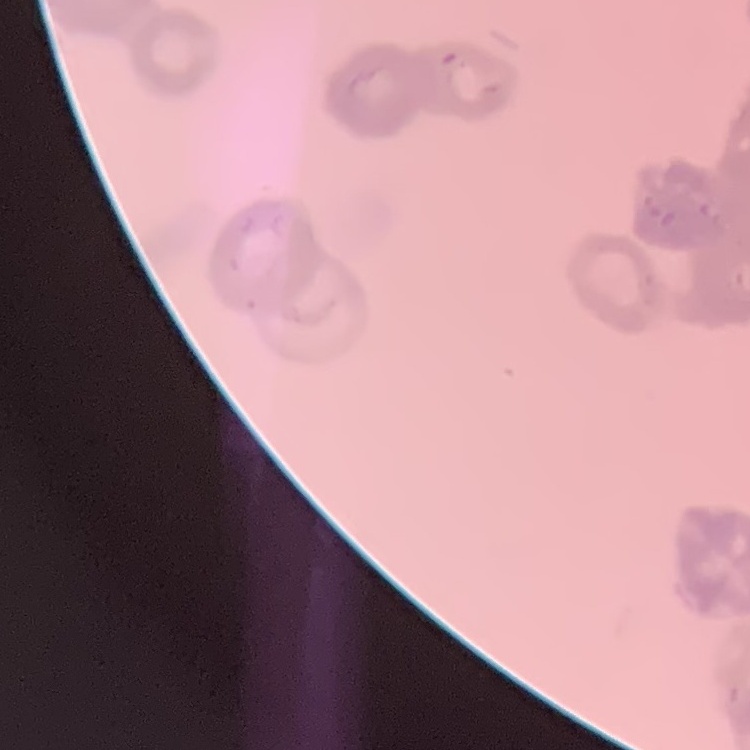
Summary:
  - Red blood cell morphology: rouleaux formation
  - Preparation: thin blood smear
  - Image type: one tile cut from a larger photomicrograph
  - Stain: Field's or Giemsa